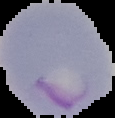
Result: malaria parasites detected. Image is 115×118 pixels. Cell region segmented out of the field of view; the surrounding area is masked to black. From a thin blood smear.